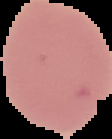
Image is 112×139 pixels. Malaria status: uninfected. From a thin blood smear. Cell region segmented out of the field of view; the surrounding area is masked to black.